Assess this cell for malaria.
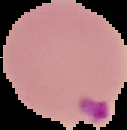

Parasitized.

Summary:
  - Image size: 127×130 pixels
  - Image type: segmented cell region on a black background
  - Preparation: thin blood smear